Report the malaria status of this cell.
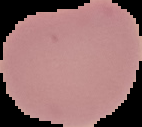

It is uninfected.

Image is 142×127 pixels. From a thin blood film. Segmented cell region on a black background.